Report the malaria status of this cell.
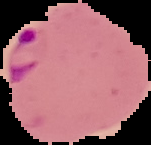

Parasitized.

Summary:
  - Image size: 151×145 pixels
  - Image type: segmented cell region on a black background
  - Preparation: thin blood smear